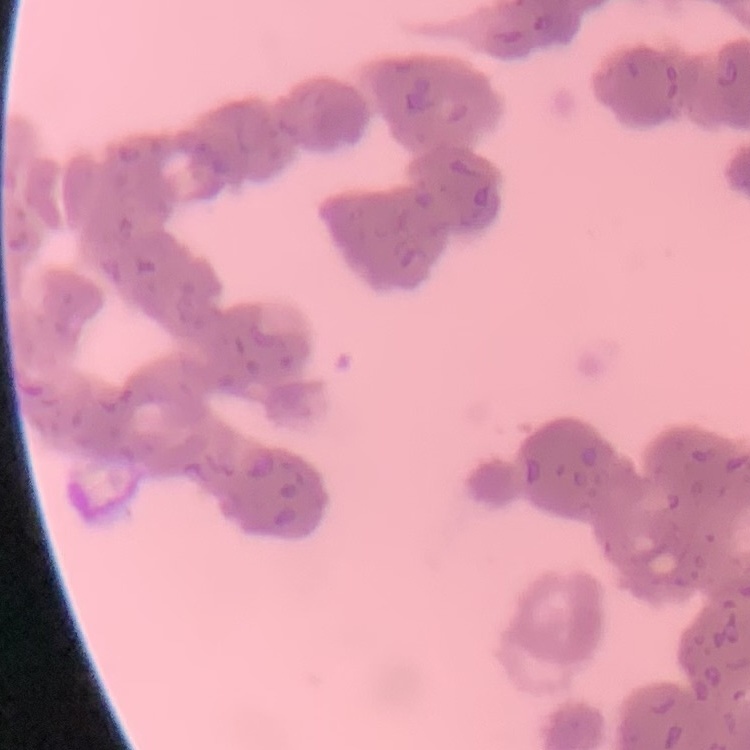
The erythrocytes show rouleaux formation. One tile cut from a larger photomicrograph. Thin blood film. Stained with either Field's or Giemsa.